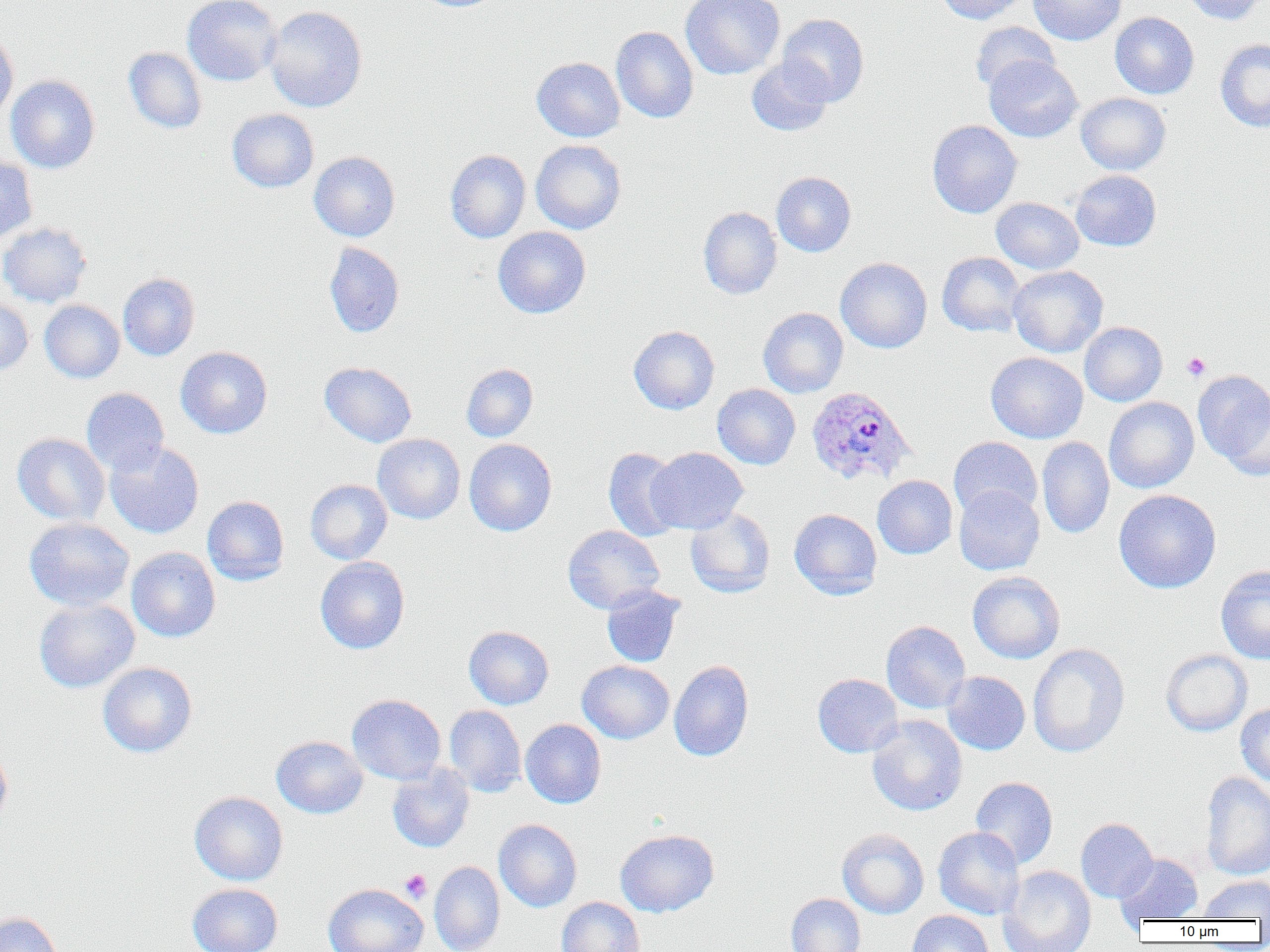 Approximate bounding boxes as named x1/y1/x2/y2 corners in pixels. Uninfected red blood cell locations: (x1=182, y1=0, x2=283, y2=86), (x1=680, y1=0, x2=785, y2=80), (x1=937, y1=0, x2=1030, y2=24), (x1=1028, y1=0, x2=1126, y2=46), (x1=1180, y1=0, x2=1266, y2=25), (x1=264, y1=5, x2=367, y2=112), (x1=1110, y1=11, x2=1199, y2=99), (x1=777, y1=14, x2=869, y2=107), (x1=970, y1=21, x2=1060, y2=94), (x1=611, y1=26, x2=698, y2=123), (x1=0, y1=30, x2=18, y2=126), (x1=1215, y1=39, x2=1270, y2=132), (x1=123, y1=47, x2=207, y2=134), (x1=984, y1=55, x2=1082, y2=142), (x1=532, y1=57, x2=625, y2=142), (x1=746, y1=58, x2=834, y2=136), (x1=6, y1=74, x2=100, y2=173), (x1=1076, y1=92, x2=1171, y2=175), (x1=227, y1=108, x2=319, y2=193), (x1=927, y1=120, x2=1022, y2=218), (x1=531, y1=140, x2=627, y2=234), (x1=445, y1=149, x2=531, y2=243), (x1=309, y1=151, x2=400, y2=242), (x1=0, y1=156, x2=37, y2=244), (x1=1070, y1=170, x2=1161, y2=251), (x1=771, y1=171, x2=856, y2=257), (x1=991, y1=197, x2=1084, y2=274), (x1=698, y1=207, x2=782, y2=299), (x1=0, y1=222, x2=92, y2=308), (x1=493, y1=227, x2=591, y2=319), (x1=324, y1=242, x2=405, y2=338), (x1=937, y1=252, x2=1026, y2=337), (x1=835, y1=257, x2=932, y2=353), (x1=1008, y1=265, x2=1108, y2=357), (x1=118, y1=273, x2=199, y2=361), (x1=0, y1=296, x2=33, y2=376), (x1=39, y1=300, x2=124, y2=383), (x1=758, y1=307, x2=848, y2=398), (x1=1079, y1=321, x2=1167, y2=406), (x1=629, y1=325, x2=720, y2=414), (x1=175, y1=346, x2=273, y2=439), (x1=986, y1=352, x2=1088, y2=443), (x1=320, y1=362, x2=417, y2=447), (x1=462, y1=363, x2=538, y2=442), (x1=1194, y1=371, x2=1270, y2=475), (x1=712, y1=384, x2=800, y2=469), (x1=81, y1=387, x2=169, y2=475), (x1=1104, y1=397, x2=1199, y2=493), (x1=12, y1=433, x2=110, y2=526), (x1=372, y1=434, x2=466, y2=524), (x1=948, y1=437, x2=1042, y2=521), (x1=1037, y1=437, x2=1115, y2=538), (x1=464, y1=439, x2=557, y2=536), (x1=105, y1=441, x2=204, y2=538), (x1=603, y1=447, x2=683, y2=541), (x1=646, y1=447, x2=748, y2=534), (x1=872, y1=475, x2=957, y2=559), (x1=305, y1=479, x2=392, y2=564), (x1=954, y1=485, x2=1044, y2=575), (x1=1114, y1=489, x2=1221, y2=593), (x1=202, y1=495, x2=289, y2=585), (x1=685, y1=508, x2=775, y2=598), (x1=789, y1=509, x2=882, y2=600), (x1=24, y1=517, x2=134, y2=611), (x1=563, y1=525, x2=665, y2=614), (x1=126, y1=547, x2=221, y2=642), (x1=314, y1=557, x2=410, y2=654), (x1=1216, y1=565, x2=1270, y2=664), (x1=967, y1=571, x2=1065, y2=664), (x1=601, y1=585, x2=686, y2=667), (x1=33, y1=598, x2=140, y2=692), (x1=881, y1=620, x2=970, y2=714), (x1=463, y1=626, x2=554, y2=709), (x1=1027, y1=643, x2=1130, y2=757), (x1=1161, y1=649, x2=1252, y2=736), (x1=577, y1=660, x2=674, y2=744), (x1=669, y1=660, x2=754, y2=762), (x1=97, y1=662, x2=197, y2=758), (x1=942, y1=671, x2=1030, y2=755), (x1=812, y1=673, x2=903, y2=757), (x1=347, y1=694, x2=446, y2=785), (x1=1236, y1=704, x2=1270, y2=786), (x1=444, y1=705, x2=526, y2=797), (x1=867, y1=715, x2=967, y2=816), (x1=520, y1=719, x2=606, y2=808), (x1=271, y1=735, x2=368, y2=818), (x1=0, y1=742, x2=13, y2=832), (x1=387, y1=763, x2=475, y2=852), (x1=1200, y1=772, x2=1270, y2=880), (x1=970, y1=777, x2=1058, y2=869), (x1=189, y1=791, x2=288, y2=885), (x1=1076, y1=818, x2=1157, y2=903), (x1=494, y1=819, x2=582, y2=912), (x1=933, y1=827, x2=1025, y2=920), (x1=615, y1=829, x2=719, y2=916), (x1=837, y1=829, x2=929, y2=919), (x1=1115, y1=853, x2=1202, y2=925), (x1=429, y1=861, x2=505, y2=952), (x1=998, y1=865, x2=1096, y2=952), (x1=1200, y1=876, x2=1270, y2=919), (x1=187, y1=882, x2=283, y2=952), (x1=323, y1=883, x2=427, y2=952), (x1=786, y1=893, x2=865, y2=952), (x1=557, y1=897, x2=645, y2=952), (x1=907, y1=910, x2=995, y2=952), (x1=0, y1=912, x2=63, y2=952). Platelet locations: (x1=1182, y1=352, x2=1210, y2=380), (x1=400, y1=869, x2=432, y2=903). Plasmodium ovale-infected red blood cell locations: (x1=806, y1=386, x2=916, y2=488). Slide-level diagnosis: Plasmodium ovale. Thin blood film. Optical microscopy. 1000x magnification. One field of a larger specimen. Image is 1270×952 pixels.